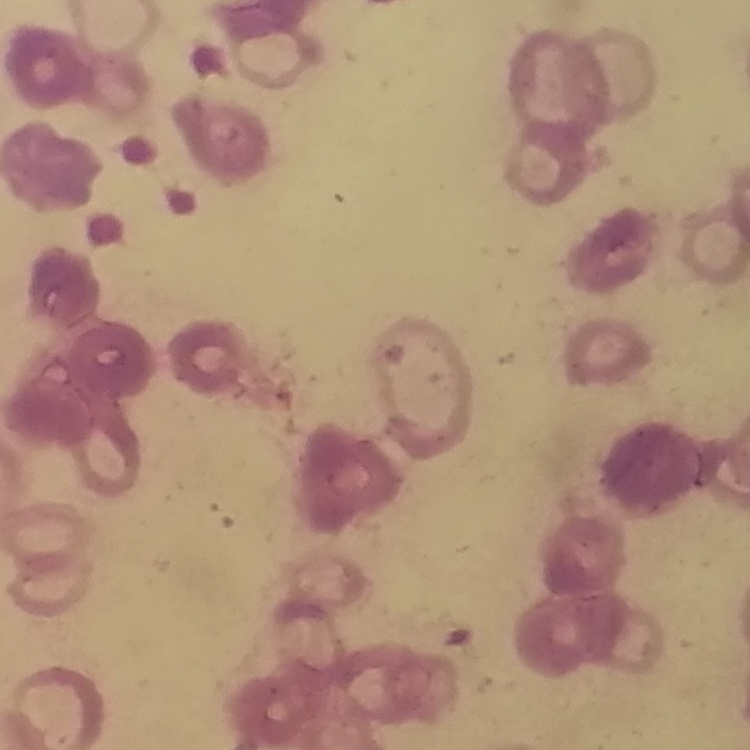

Summary:
  - Erythrocyte morphology: rouleaux formation
  - Image type: square crop of a larger photomicrograph
  - Preparation: thin peripheral smear
  - Stain: Field's or Giemsa